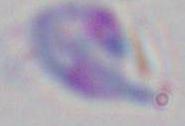
modality = photomicrograph
magnification = 1000x
identification = Toxoplasma gondii